Assess the morphology of the red blood cells.
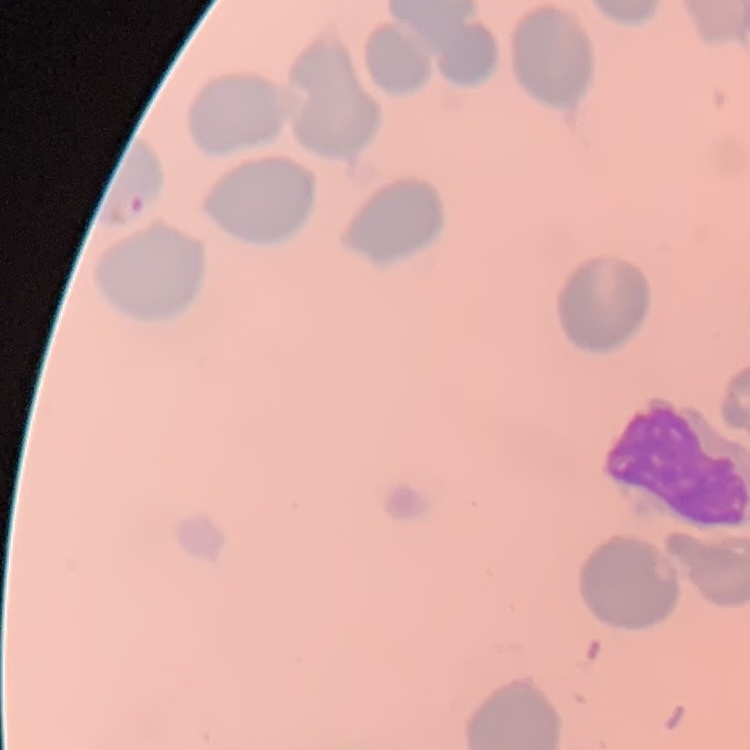

They show no rouleaux formation.

preparation = thin peripheral smear
image type = one tile cut from a larger photomicrograph
stain = Field's or Giemsa